Report the malaria status of this cell.
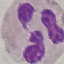

Uninfected.

Photographed with a smartphone camera at the microscope eyepiece. Giemsa stain. Thin blood smear. Automatically extracted cell patch, resized to 64 × 64 pixels.